Comment on the morphology of the erythrocytes.
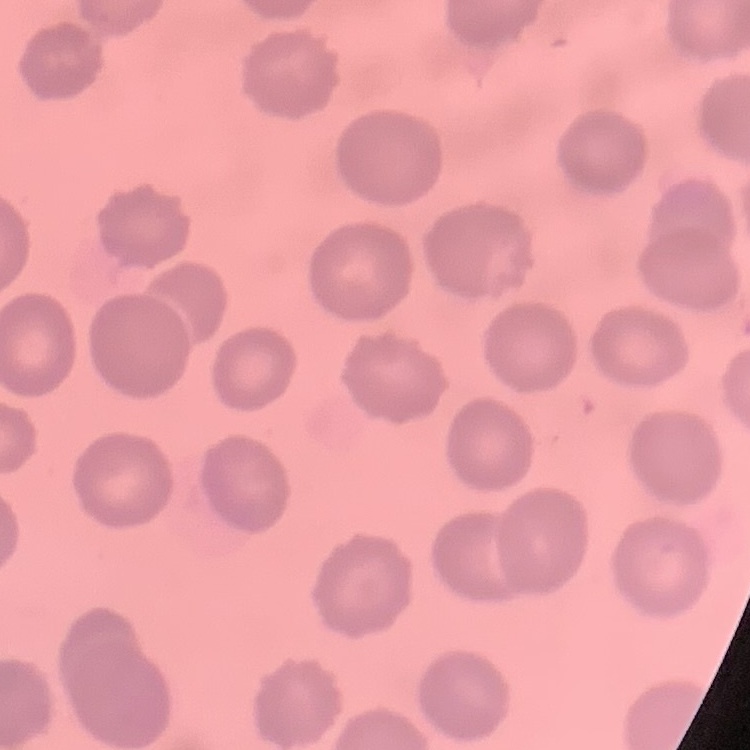

They show no rouleaux formation.

stain = Field's or Giemsa
preparation = thin blood smear
image type = square crop of a larger photomicrograph